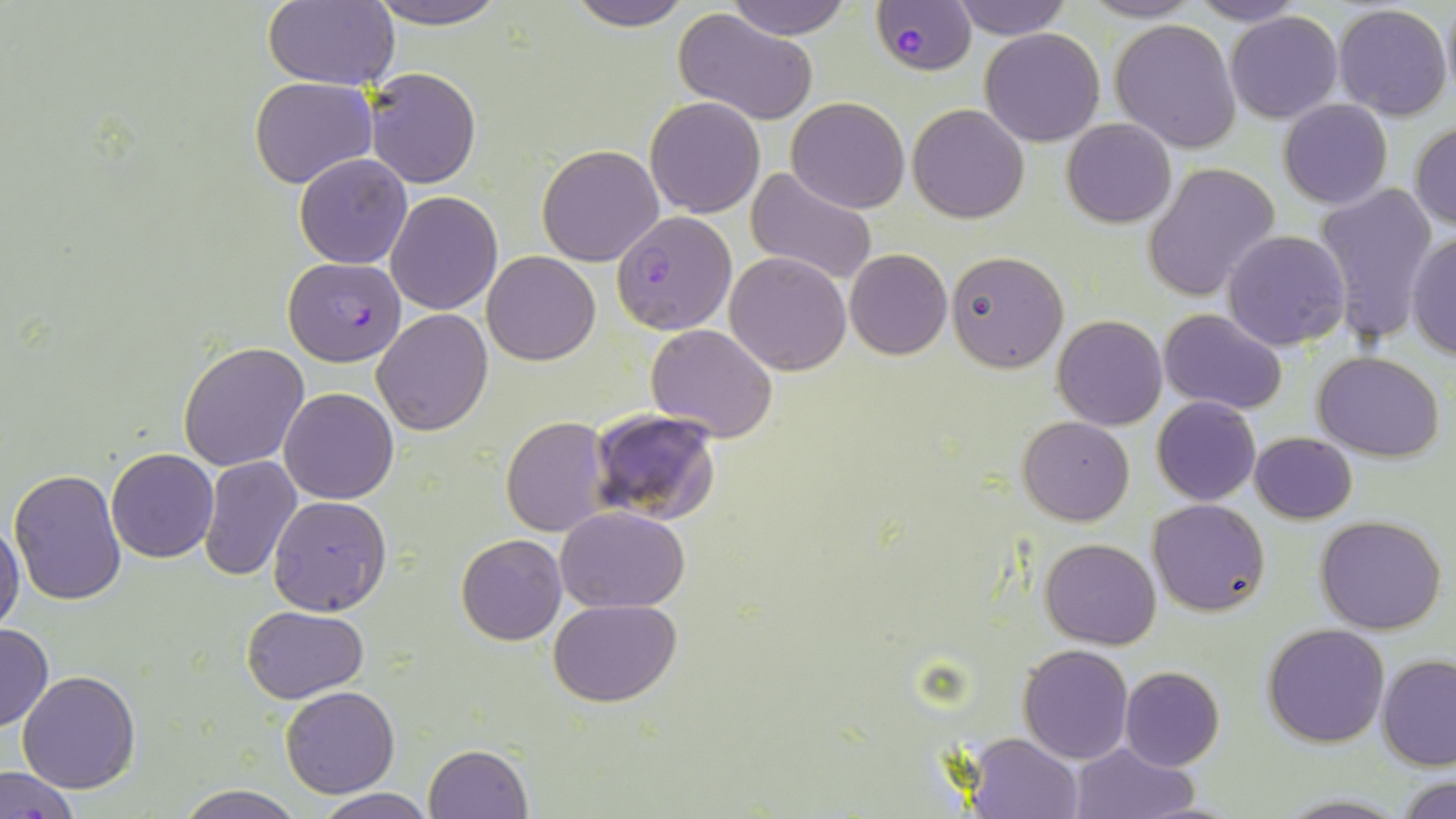

Summary:
  - Coordinate format: approximate bounding boxes as named x1/y1/x2/y2 corners in pixels
  - Plasmodium falciparum-infected red blood cell locations: (x1=873, y1=0, x2=976, y2=76), (x1=611, y1=211, x2=736, y2=335), (x1=283, y1=257, x2=407, y2=366)
  - Uninfected red blood cell locations: (x1=262, y1=0, x2=400, y2=90), (x1=358, y1=0, x2=515, y2=27), (x1=565, y1=0, x2=694, y2=31), (x1=721, y1=0, x2=859, y2=40), (x1=950, y1=0, x2=1073, y2=40), (x1=1078, y1=0, x2=1204, y2=23), (x1=1186, y1=0, x2=1308, y2=26), (x1=1440, y1=0, x2=1455, y2=103), (x1=1333, y1=3, x2=1453, y2=120), (x1=673, y1=11, x2=818, y2=127), (x1=1225, y1=12, x2=1343, y2=123), (x1=1109, y1=19, x2=1242, y2=154), (x1=980, y1=27, x2=1105, y2=147), (x1=363, y1=67, x2=483, y2=188), (x1=249, y1=77, x2=378, y2=189), (x1=646, y1=95, x2=764, y2=219), (x1=786, y1=97, x2=910, y2=215), (x1=1279, y1=100, x2=1391, y2=209), (x1=908, y1=103, x2=1030, y2=222), (x1=1061, y1=118, x2=1177, y2=228), (x1=1410, y1=121, x2=1456, y2=231), (x1=537, y1=143, x2=664, y2=266), (x1=294, y1=153, x2=414, y2=269), (x1=1143, y1=162, x2=1280, y2=302), (x1=746, y1=167, x2=878, y2=287), (x1=291, y1=170, x2=498, y2=291), (x1=1314, y1=181, x2=1439, y2=345), (x1=386, y1=191, x2=503, y2=315), (x1=1222, y1=230, x2=1350, y2=351), (x1=1406, y1=233, x2=1456, y2=360), (x1=845, y1=248, x2=951, y2=361), (x1=944, y1=250, x2=1068, y2=372), (x1=483, y1=251, x2=599, y2=365), (x1=724, y1=251, x2=852, y2=375), (x1=371, y1=308, x2=493, y2=436), (x1=1160, y1=309, x2=1288, y2=415), (x1=1052, y1=315, x2=1167, y2=430), (x1=647, y1=325, x2=778, y2=442), (x1=178, y1=341, x2=310, y2=471), (x1=1313, y1=351, x2=1445, y2=459), (x1=278, y1=387, x2=399, y2=505), (x1=1152, y1=397, x2=1260, y2=506), (x1=589, y1=408, x2=722, y2=525), (x1=1018, y1=416, x2=1135, y2=526), (x1=501, y1=417, x2=610, y2=536), (x1=1250, y1=432, x2=1357, y2=523), (x1=106, y1=448, x2=219, y2=562), (x1=198, y1=455, x2=302, y2=582), (x1=8, y1=467, x2=128, y2=606), (x1=268, y1=494, x2=392, y2=615), (x1=1149, y1=499, x2=1271, y2=618), (x1=556, y1=505, x2=692, y2=612), (x1=1314, y1=515, x2=1447, y2=634), (x1=0, y1=517, x2=25, y2=634), (x1=455, y1=533, x2=567, y2=646), (x1=1041, y1=538, x2=1161, y2=650), (x1=548, y1=598, x2=681, y2=707), (x1=242, y1=605, x2=367, y2=703), (x1=0, y1=623, x2=52, y2=732), (x1=1263, y1=623, x2=1390, y2=748), (x1=1018, y1=644, x2=1133, y2=764), (x1=1377, y1=654, x2=1456, y2=771), (x1=1120, y1=665, x2=1223, y2=770), (x1=18, y1=671, x2=141, y2=793), (x1=280, y1=686, x2=400, y2=798), (x1=963, y1=731, x2=1084, y2=819), (x1=1067, y1=741, x2=1202, y2=818), (x1=424, y1=744, x2=532, y2=819), (x1=1, y1=763, x2=81, y2=819), (x1=1398, y1=776, x2=1455, y2=817), (x1=176, y1=783, x2=304, y2=819), (x1=312, y1=789, x2=436, y2=818)
  - Slide-level diagnosis: Plasmodium falciparum
  - Field of view: single
  - Image size: 1456×819 pixels
  - Modality: optical microscopy
  - Stain: May-Grünwald-Giemsa
  - Magnification: 1000x
  - Preparation: thin blood smear